Name the parasite shown.
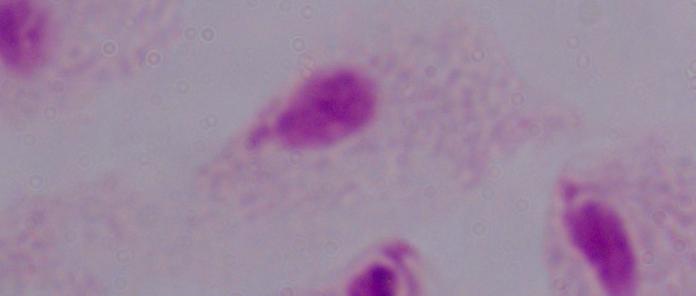

A trichomonad.

magnification = 1000x
modality = photomicrograph